Describe the morphology of the erythrocytes.
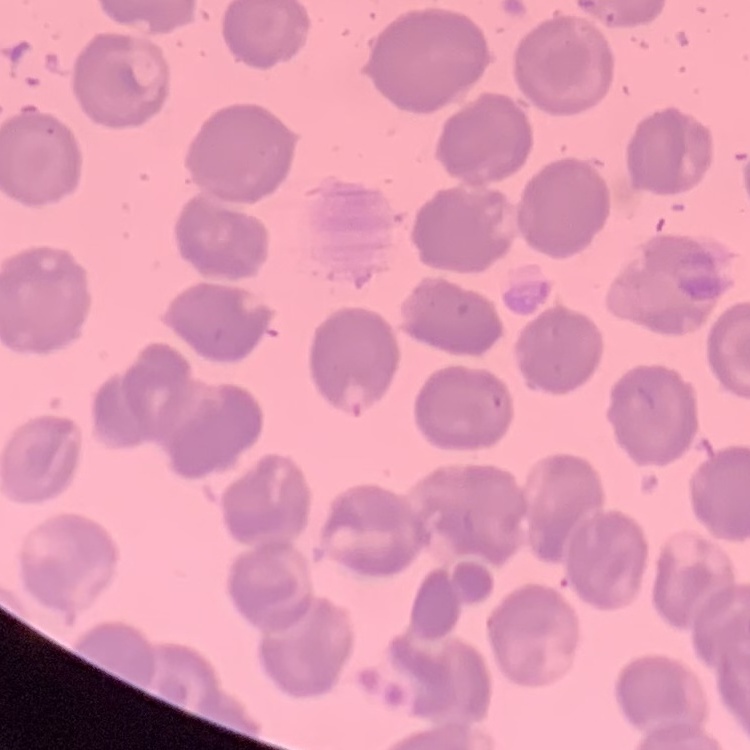
They show no rouleaux formation.

stain = Field's or Giemsa
image type = square crop of a larger photomicrograph
preparation = thin blood film